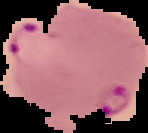
From a thin blood film. Image is 148×133 pixels. Result: Plasmodium parasites detected. The area outside the segmented cell region is set to black.